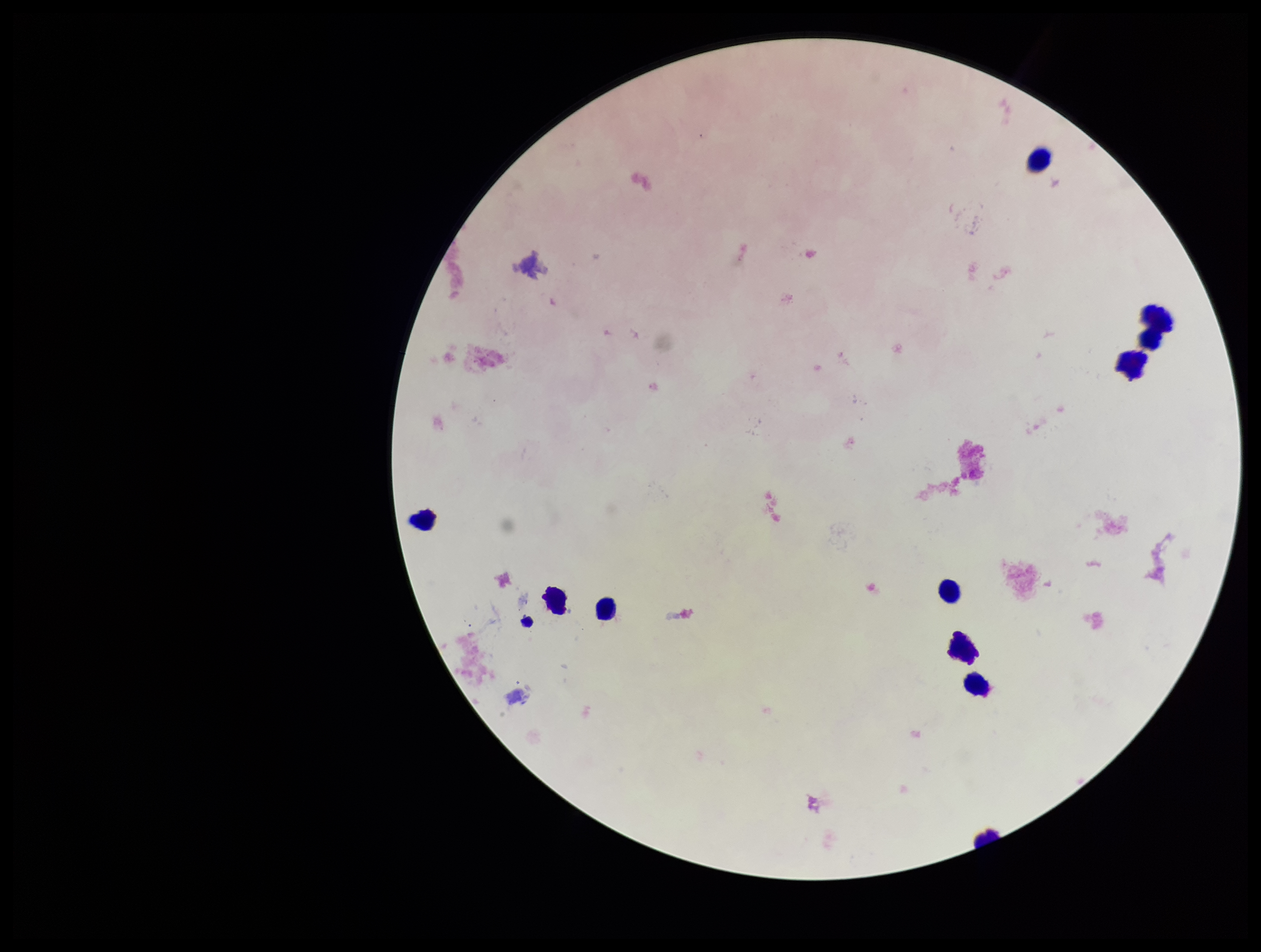
leukocyte count = 10
preparation = thick blood smear
field of view = single
parasite count = 0
image size = 1261×952 pixels
patient malaria status = negative
capture = smartphone photograph through the microscope eyepiece
stain = Giemsa
Plasmodium parasites = none identified